Identify the blood parasite species.
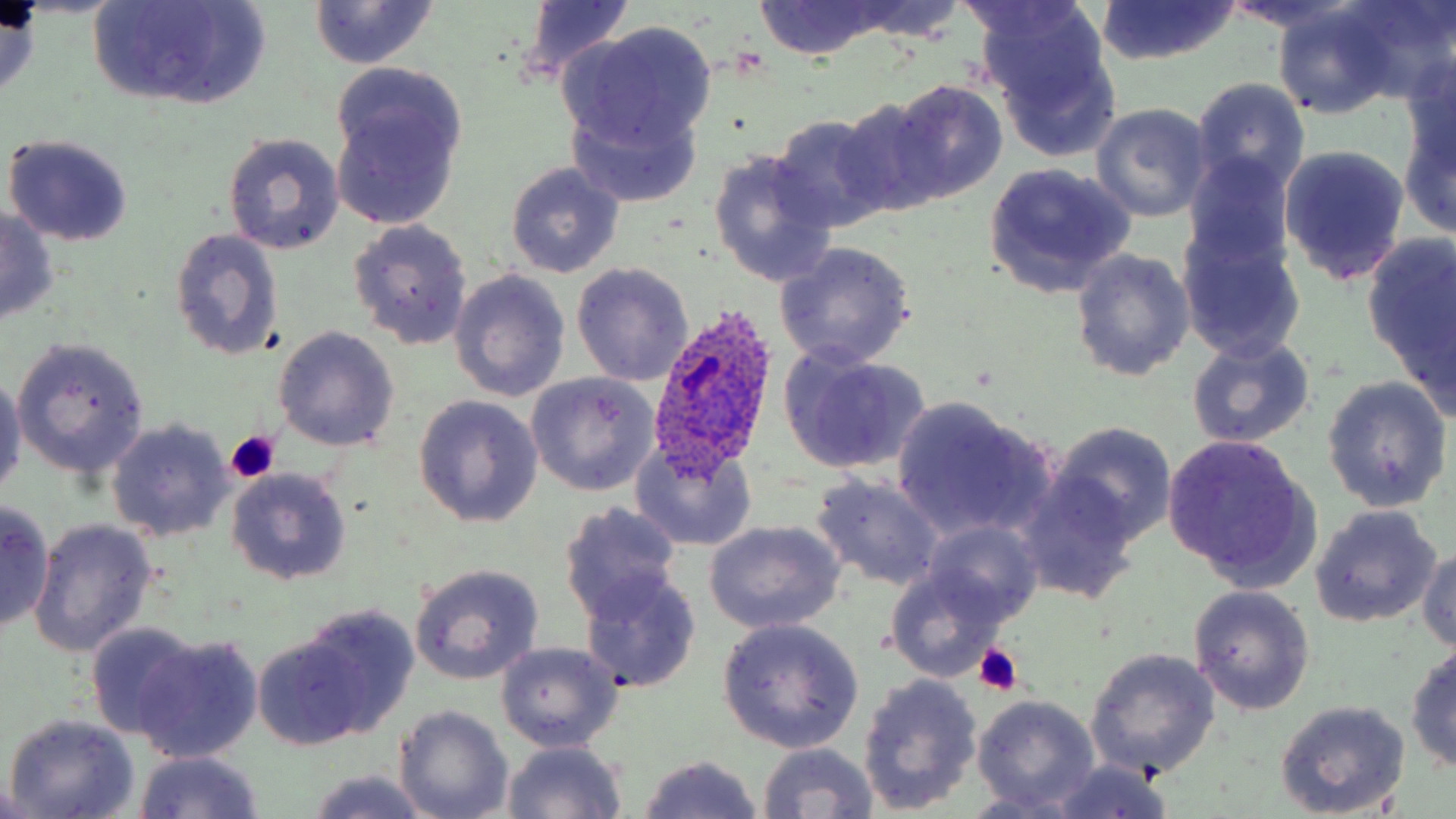
Plasmodium ovale.

Approximate bounding boxes as (x1,y1)-(x2,y2) corner pairs in pixels. Platelet locations: (226,432)-(280,480), (972,643)-(1023,695). Uninfected red blood cell locations: (511,0)-(640,84), (753,0)-(894,60), (840,0)-(966,40), (1339,0)-(1456,104), (88,1)-(272,112), (1094,1)-(1242,65), (1218,1)-(1364,38), (309,2)-(440,69), (0,4)-(42,96), (1272,4)-(1401,121), (977,7)-(1122,151), (559,25)-(719,155), (328,68)-(469,229), (1191,77)-(1310,199), (887,80)-(1007,204), (831,93)-(948,220), (568,97)-(702,207), (1091,104)-(1214,221), (1397,108)-(1456,237), (1025,111)-(1194,253), (768,113)-(897,235), (222,133)-(346,256), (3,134)-(136,248), (1278,143)-(1411,288), (706,150)-(839,289), (1184,153)-(1294,270), (506,162)-(624,276), (982,162)-(1137,298), (0,208)-(60,326), (348,220)-(473,349), (1178,225)-(1305,361), (169,228)-(284,363), (1365,234)-(1456,390), (776,242)-(916,369), (1070,249)-(1194,381), (570,264)-(692,387), (449,266)-(572,401), (274,327)-(399,451), (1186,335)-(1316,449), (13,337)-(151,478), (778,349)-(931,473), (0,373)-(24,498), (524,373)-(659,496), (1321,379)-(1450,510), (414,396)-(544,527), (892,397)-(1058,546), (107,420)-(235,540), (1051,421)-(1178,545), (1161,434)-(1319,592), (630,441)-(759,552), (225,467)-(353,585), (811,474)-(945,592), (1014,475)-(1140,603), (0,499)-(53,630), (560,502)-(685,622), (1309,504)-(1442,628), (29,519)-(157,658), (702,521)-(845,636), (922,521)-(1043,627), (1418,547)-(1456,653), (884,562)-(1010,681), (410,563)-(544,684), (581,569)-(701,694), (1188,585)-(1315,713), (298,606)-(419,737), (717,619)-(864,753), (86,621)-(201,738), (133,634)-(262,763), (253,634)-(371,751), (495,642)-(623,751), (1405,643)-(1456,770), (1086,648)-(1221,778), (858,674)-(982,813), (972,695)-(1101,812), (1275,701)-(1409,816), (395,706)-(512,819), (4,714)-(140,819), (502,740)-(627,818), (757,742)-(880,819), (132,750)-(265,819), (636,755)-(764,818), (1046,762)-(1174,819), (307,771)-(430,818), (0,782)-(45,817). Plasmodium ovale-infected red blood cell locations: (649,307)-(778,475). 1000x magnification. Thin blood smear. May-Grünwald-Giemsa stain. Optical microscopy. Single field of view. Image is 1456×819 pixels.